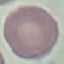
Malaria status: uninfected. Automatically extracted cell patch, resized to 64 × 64 pixels. Giemsa stain. Thin blood film. Acquired by smartphone through the microscope eyepiece.